State which cell type is depicted.
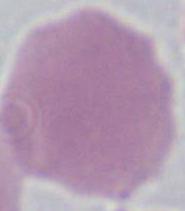

An erythrocyte.

magnification = 1000x
modality = micrograph